Comment on the morphology of the red blood cells.
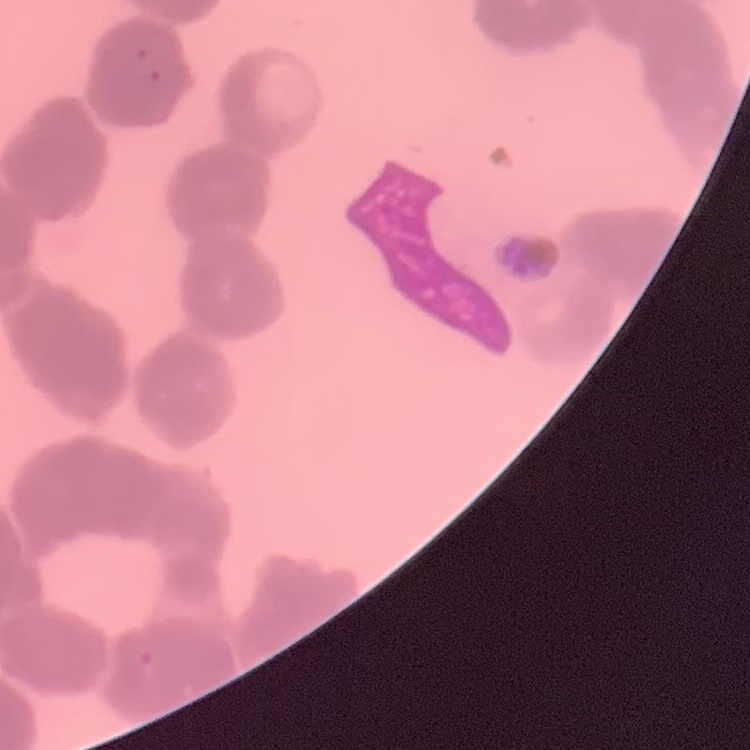

They show rouleaux formation.

{
  "image_type": "square crop of a larger photomicrograph",
  "stain": "Field's or Giemsa",
  "preparation": "thin blood smear"
}